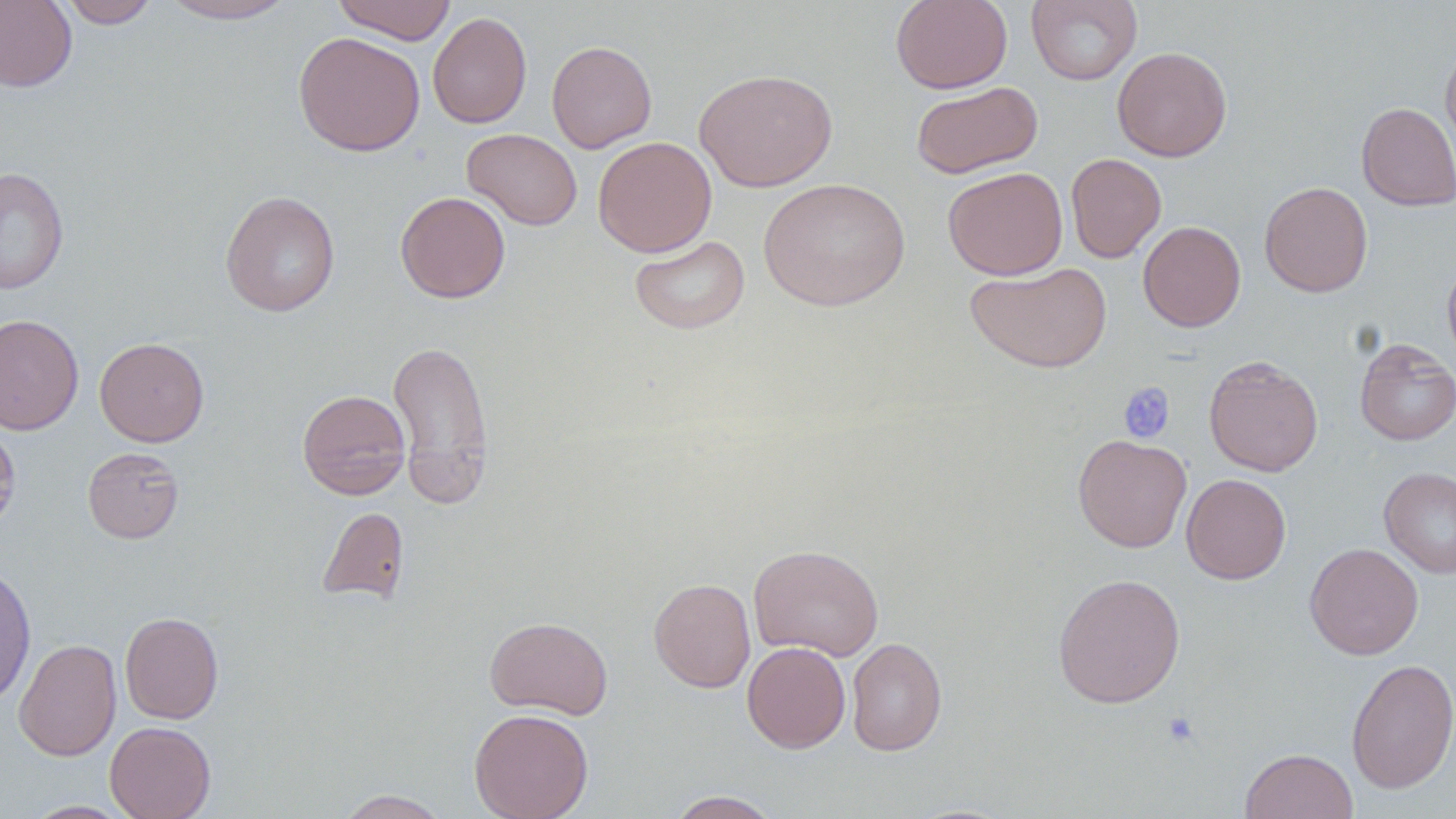

Approximate bounding boxes as (x1,y1)-(x2,y2) corner pairs in pixels. Platelet locations: (1118,381)-(1176,444), (1162,711)-(1200,748). Uninfected red blood cell locations: (0,0)-(76,92), (56,0)-(160,28), (160,0)-(297,23), (332,0)-(457,44), (890,0)-(1013,94), (1025,0)-(1143,86), (428,11)-(531,128), (293,31)-(426,157), (546,40)-(657,153), (1440,42)-(1456,162), (1112,46)-(1232,161), (694,67)-(838,192), (911,81)-(1043,179), (1356,102)-(1456,211), (461,128)-(583,231), (593,136)-(716,257), (1065,153)-(1167,263), (1,166)-(69,295), (943,166)-(1068,280), (757,177)-(911,311), (1259,181)-(1373,297), (220,190)-(341,317), (395,191)-(510,303), (1137,221)-(1246,332), (629,235)-(750,334), (1442,255)-(1456,373), (966,262)-(1111,373), (0,313)-(84,435), (95,337)-(209,447), (388,337)-(494,506), (1354,338)-(1456,445), (1204,355)-(1323,477), (297,389)-(411,499), (0,422)-(21,535), (1073,434)-(1192,552), (83,447)-(184,543), (1378,466)-(1456,578), (1181,473)-(1291,584), (317,506)-(410,604), (1304,542)-(1424,660), (749,544)-(884,661), (0,564)-(36,706), (1052,572)-(1186,708), (649,577)-(756,693), (120,611)-(223,724), (484,615)-(613,719), (846,637)-(947,756), (14,638)-(122,761), (742,642)-(850,753), (1346,658)-(1456,794), (469,708)-(594,819), (105,721)-(215,819), (1240,748)-(1358,819), (336,789)-(450,818), (665,790)-(783,818), (24,800)-(133,818). Slide-level diagnosis: negative for blood parasites. One field of a larger specimen. Captured at 1000x magnification. Thin blood smear. Image is 1456×819 pixels. May-Grünwald-Giemsa stain. Light microscopy.